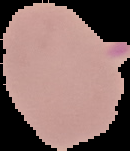

Summary:
  - Malaria status: uninfected
  - Preparation: thin blood smear
  - Image type: segmented cell region on a black background
  - Image size: 130×151 pixels